Classify this cell by malaria status.
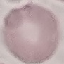

It is uninfected.

{
  "stain": "Giemsa",
  "preparation": "thin blood film",
  "capture": "smartphone camera at the microscope eyepiece",
  "image_type": "automatically extracted cell patch, resized to 64 × 64 pixels"
}